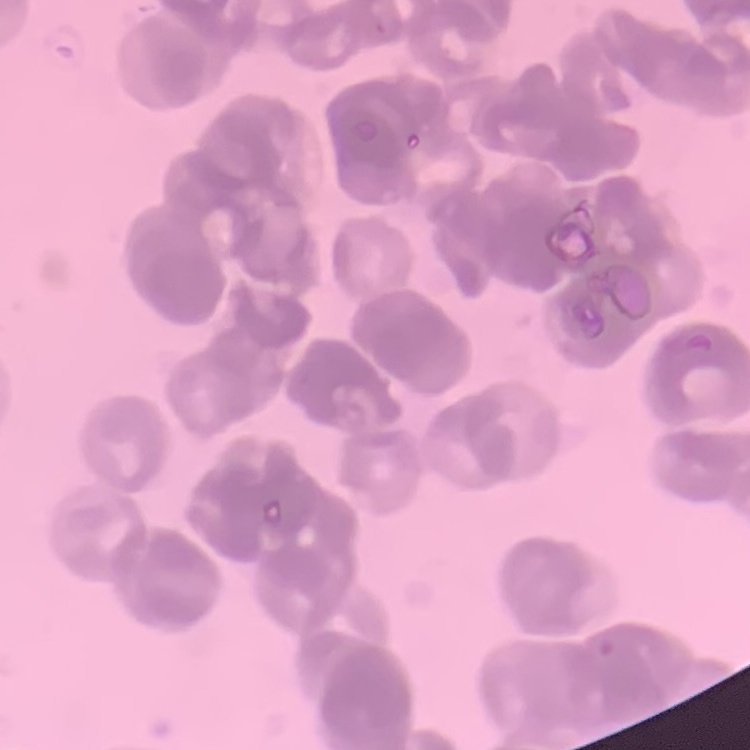

erythrocyte morphology = rouleaux formation
image type = square crop of a larger photomicrograph
preparation = thin blood smear
stain = Field's or Giemsa